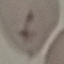 Result: negative for malaria parasites. Giemsa-stained preparation. Cell patch, automatically extracted from a larger field of view and resized to 64 × 64 pixels. Acquired by smartphone through the microscope eyepiece. Thin blood film.